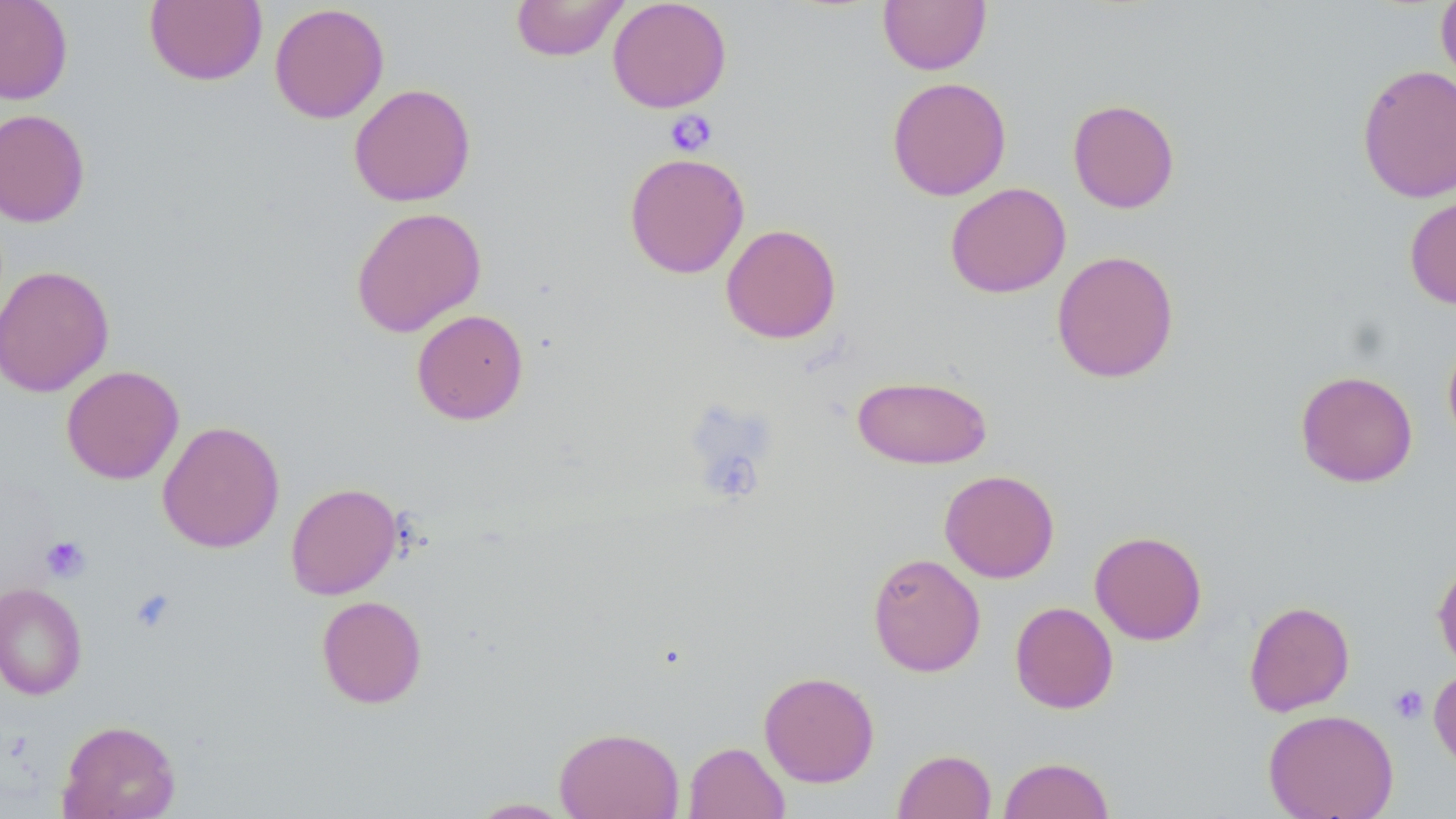

Summary:
  - Coordinate format: approximate bounding boxes as [x1, y1, x2, y2] in pixels
  - Uninfected red blood cell locations: [0, 0, 73, 104], [144, 0, 267, 87], [510, 0, 628, 61], [607, 0, 732, 113], [878, 0, 991, 75], [1435, 0, 1456, 93], [269, 3, 389, 124], [1356, 64, 1456, 203], [886, 76, 1012, 201], [349, 83, 476, 207], [1067, 98, 1180, 214], [0, 108, 91, 227], [624, 152, 749, 279], [945, 182, 1071, 298], [1404, 194, 1456, 310], [350, 206, 487, 337], [720, 224, 841, 344], [1051, 250, 1180, 383], [0, 264, 114, 398], [411, 309, 529, 425], [1442, 335, 1456, 452], [61, 365, 184, 485], [1295, 370, 1418, 487], [852, 374, 992, 469], [157, 421, 285, 552], [939, 469, 1059, 583], [285, 482, 401, 599], [1090, 530, 1208, 645], [867, 552, 985, 677], [1432, 558, 1456, 673], [0, 582, 88, 700], [316, 595, 428, 708], [1243, 600, 1355, 716], [1010, 601, 1118, 714], [1429, 667, 1456, 773], [758, 671, 880, 787], [1263, 709, 1399, 819], [58, 719, 181, 819], [554, 726, 684, 819], [684, 741, 789, 819], [893, 749, 996, 819], [998, 756, 1115, 819], [466, 798, 576, 818]
  - Platelet locations: [665, 111, 718, 156], [40, 535, 91, 583], [130, 588, 177, 633], [1389, 685, 1429, 724]
  - Slide-level diagnosis: no evidence of blood parasites
  - Image size: 1456×819 pixels
  - Preparation: thin blood smear
  - Magnification: 1000x
  - Stain: May-Grünwald-Giemsa
  - Field of view: one of a larger specimen
  - Modality: optical microscopy